Identify the parasite.
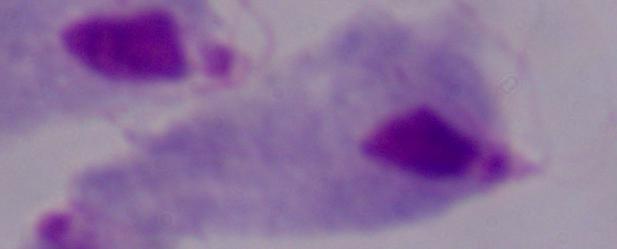

This is a trichomonad.

Summary:
  - Modality: photomicrograph
  - Magnification: 1000x